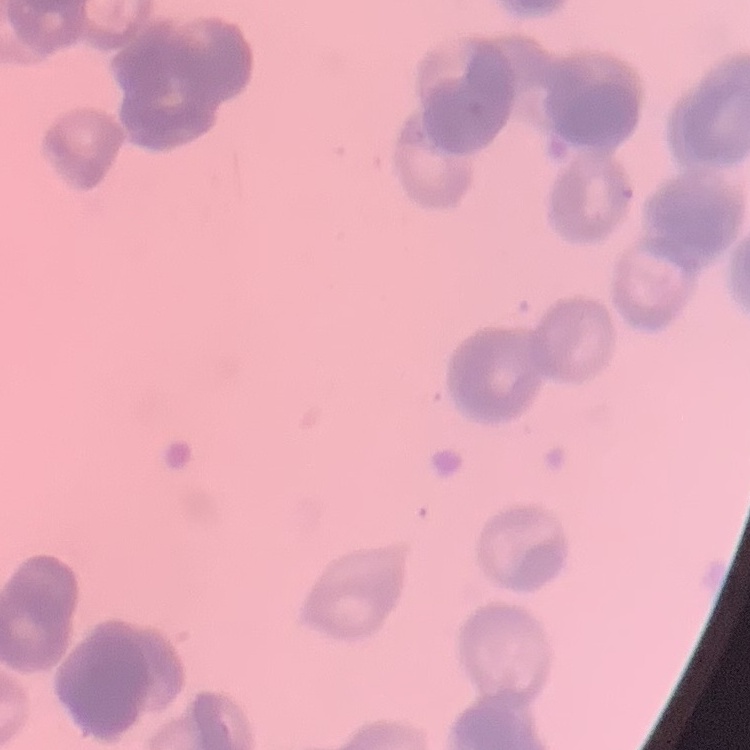

red_blood_cell_morphology: rouleaux formation
image_type: square crop of a larger photomicrograph
stain: Field's or Giemsa
preparation: thin blood smear